State which parasite is depicted.
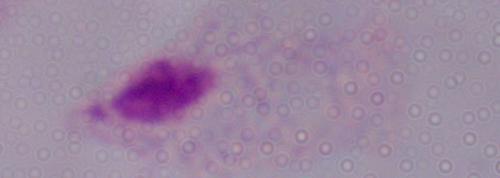

This is a trichomonad.

magnification = 1000x
modality = micrograph